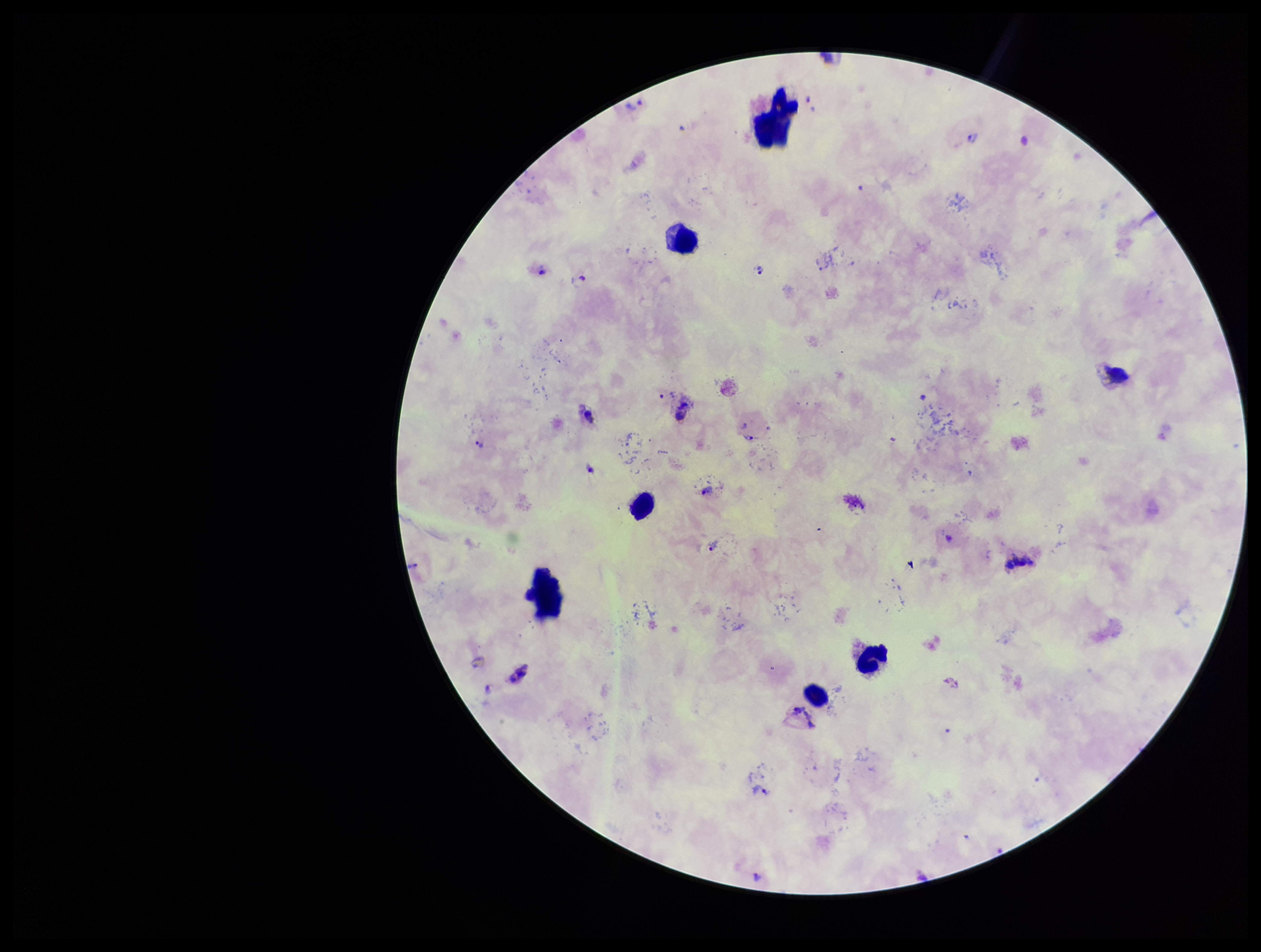

preparation: thick smear
plasmodium_parasites: seen
parasite_count: 13
stain: Giemsa
patient_malaria_status: positive
capture: smartphone photograph through the microscope eyepiece
leukocyte_count: 6
species_reported_for_this_patient: Plasmodium vivax
field_of_view: single
image_size: 1261×952 pixels